Name the parasite shown.
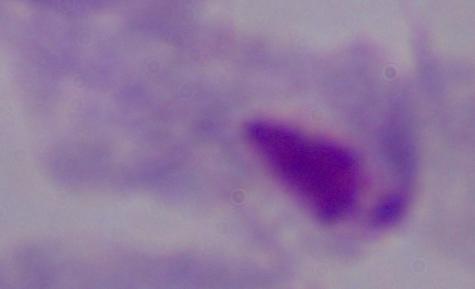
A trichomonad.

Summary:
  - Magnification: 1000x
  - Modality: photomicrograph